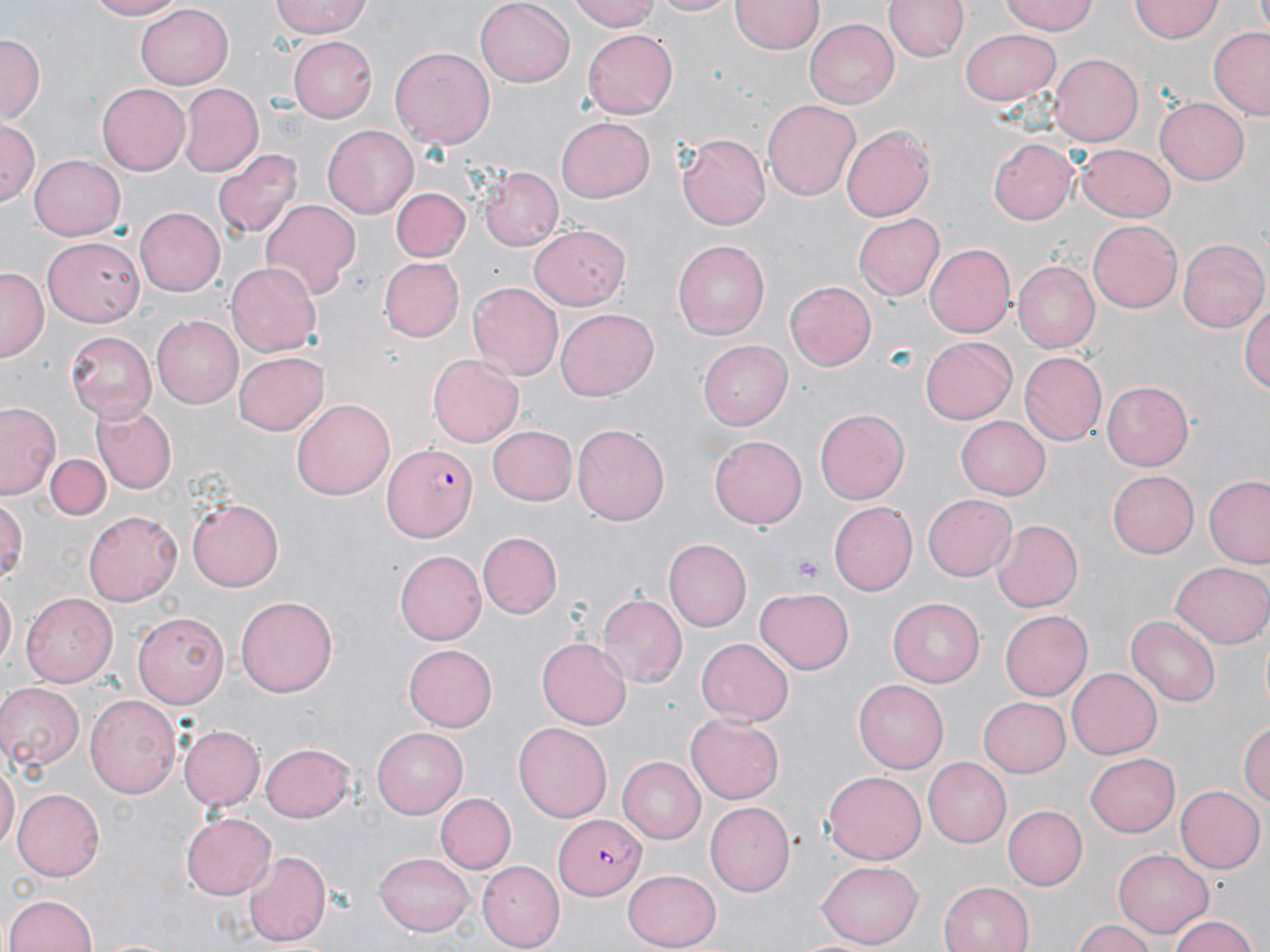
Summary:
  - Coordinate format: approximate bounding boxes as [x1, y1, x2, y2] in pixels
  - Platelet locations: [792, 554, 824, 587]
  - Uninfected red blood cell locations: [81, 0, 192, 20], [268, 0, 373, 39], [473, 0, 574, 87], [566, 0, 665, 31], [643, 0, 742, 18], [732, 0, 822, 55], [886, 0, 967, 62], [1000, 0, 1100, 36], [1131, 0, 1221, 43], [1253, 0, 1270, 36], [136, 2, 233, 85], [804, 16, 899, 106], [1208, 26, 1270, 121], [961, 27, 1062, 106], [581, 29, 676, 119], [0, 33, 43, 123], [288, 38, 376, 121], [390, 45, 495, 149], [1050, 52, 1145, 146], [178, 83, 263, 175], [97, 85, 190, 175], [1154, 95, 1250, 182], [762, 97, 861, 201], [557, 118, 655, 206], [1, 123, 40, 203], [324, 124, 418, 219], [841, 125, 936, 221], [676, 133, 770, 231], [990, 136, 1081, 226], [1077, 142, 1177, 221], [214, 149, 303, 240], [30, 153, 127, 239], [478, 168, 563, 253], [392, 185, 470, 262], [260, 199, 359, 303], [135, 207, 224, 297], [854, 214, 944, 301], [1086, 219, 1182, 314], [528, 225, 629, 308], [42, 238, 143, 328], [1178, 238, 1269, 333], [674, 240, 770, 340], [927, 242, 1016, 339], [378, 256, 462, 340], [227, 262, 321, 356], [1012, 262, 1099, 354], [0, 268, 46, 363], [785, 280, 878, 371], [468, 283, 563, 380], [1241, 296, 1270, 397], [556, 307, 658, 401], [152, 314, 243, 408], [65, 330, 156, 419], [921, 337, 1018, 424], [699, 342, 791, 430], [232, 351, 327, 436], [1019, 352, 1107, 445], [428, 354, 524, 448], [1102, 381, 1194, 472], [292, 397, 394, 500], [0, 401, 63, 500], [93, 404, 177, 492], [816, 408, 909, 505], [955, 416, 1051, 499], [487, 423, 578, 505], [572, 424, 671, 527], [711, 434, 808, 528], [46, 453, 110, 520], [1106, 469, 1199, 558], [1204, 476, 1270, 568], [923, 495, 1018, 581], [188, 496, 285, 592], [0, 498, 26, 589], [830, 501, 918, 595], [82, 510, 183, 606], [991, 519, 1082, 614], [478, 534, 561, 618], [662, 539, 751, 631], [394, 550, 486, 645], [1172, 562, 1269, 648], [0, 587, 15, 672], [755, 588, 854, 674], [22, 592, 118, 685], [597, 593, 687, 687], [234, 594, 338, 699], [889, 596, 988, 687], [1000, 608, 1095, 701], [133, 612, 228, 708], [1125, 615, 1220, 708], [537, 638, 630, 729], [697, 639, 793, 726], [404, 643, 497, 731], [1068, 669, 1160, 758], [854, 680, 948, 773], [0, 683, 86, 769], [85, 693, 181, 799], [977, 696, 1070, 777], [685, 714, 784, 805], [1239, 718, 1269, 807], [513, 722, 611, 823], [177, 724, 263, 812], [372, 727, 467, 817], [262, 740, 357, 822], [1086, 753, 1181, 837], [616, 756, 705, 844], [925, 757, 1012, 846], [0, 763, 18, 852], [824, 769, 929, 865], [1176, 784, 1264, 873], [14, 789, 105, 879], [433, 794, 515, 874], [708, 801, 795, 896], [1000, 803, 1087, 892], [181, 811, 275, 900], [1116, 848, 1213, 937], [244, 849, 332, 946], [375, 851, 476, 936], [479, 862, 565, 948], [816, 862, 924, 947], [621, 870, 721, 950], [939, 880, 1035, 952], [3, 892, 99, 952], [1166, 915, 1264, 952], [1072, 919, 1159, 952]
  - Plasmodium falciparum-infected red blood cell locations: [382, 445, 478, 542], [552, 813, 642, 900]
  - Slide-level diagnosis: Plasmodium falciparum
  - Field of view: single
  - Magnification: 1000x
  - Image size: 1270×952 pixels
  - Preparation: thin blood film
  - Stain: May-Grünwald-Giemsa
  - Modality: optical microscopy